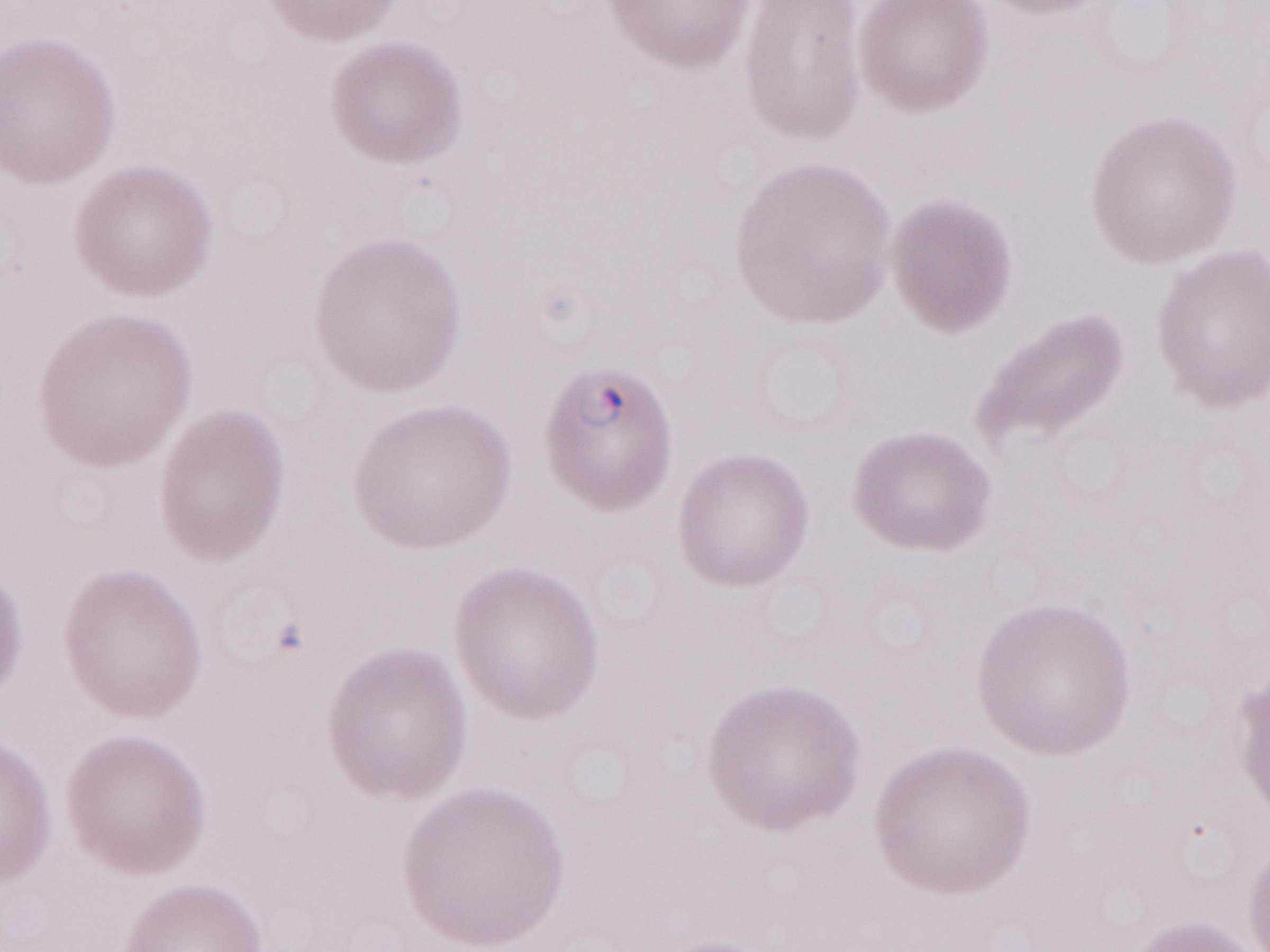
Image is 1270×952 pixels. Malaria diagnosis (patient-level): positive. Olympus BX43 microscope, Olympus DP73 camera. Thin blood film. Magnification: 1,000x. May-Grünwald-Giemsa stain. Single field of view.